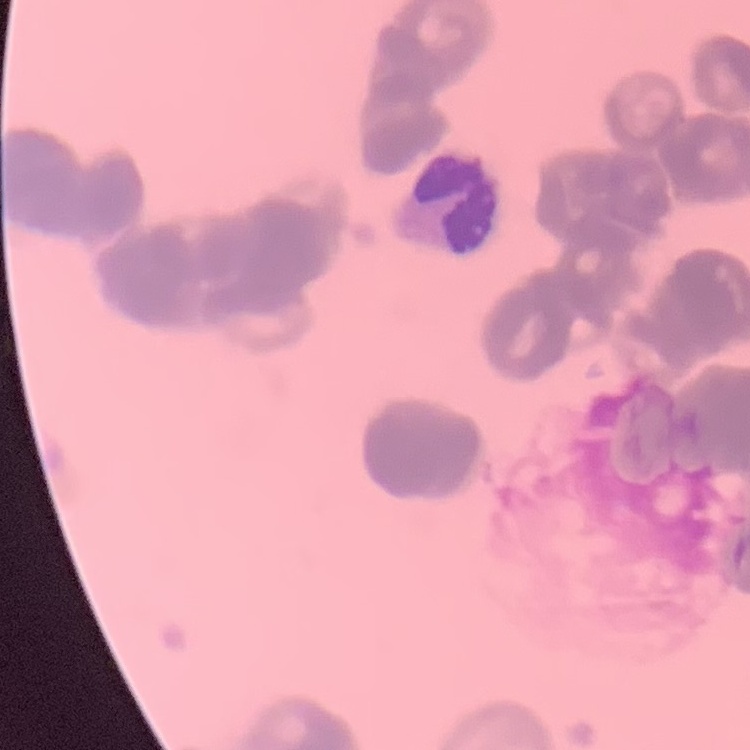
Summary:
  - Erythrocyte morphology: rouleaux formation
  - Preparation: thin blood film
  - Stain: Field's or Giemsa
  - Image type: square crop of a larger photomicrograph